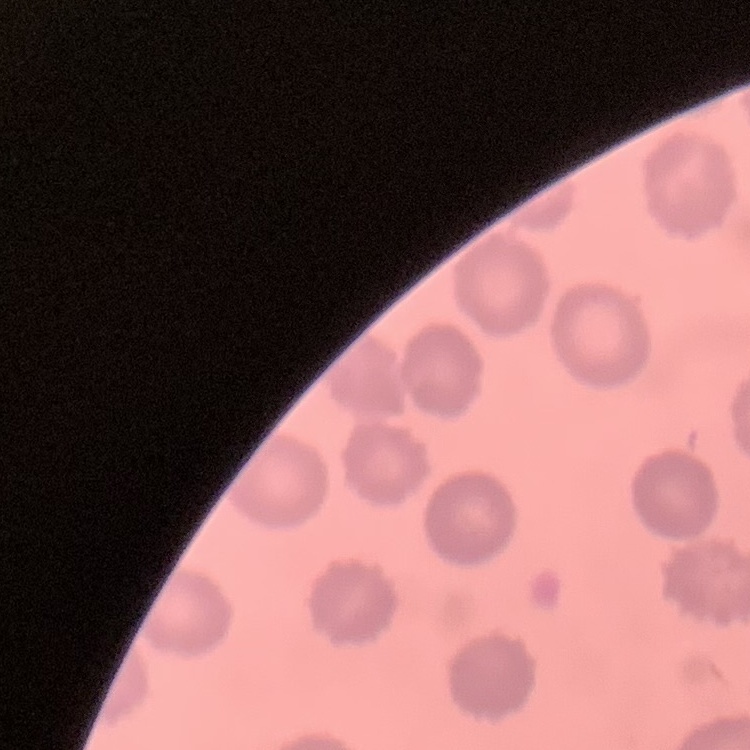 The erythrocytes show no rouleaux formation. Field's or Giemsa stain. Square crop of a larger photomicrograph. Thin peripheral smear.